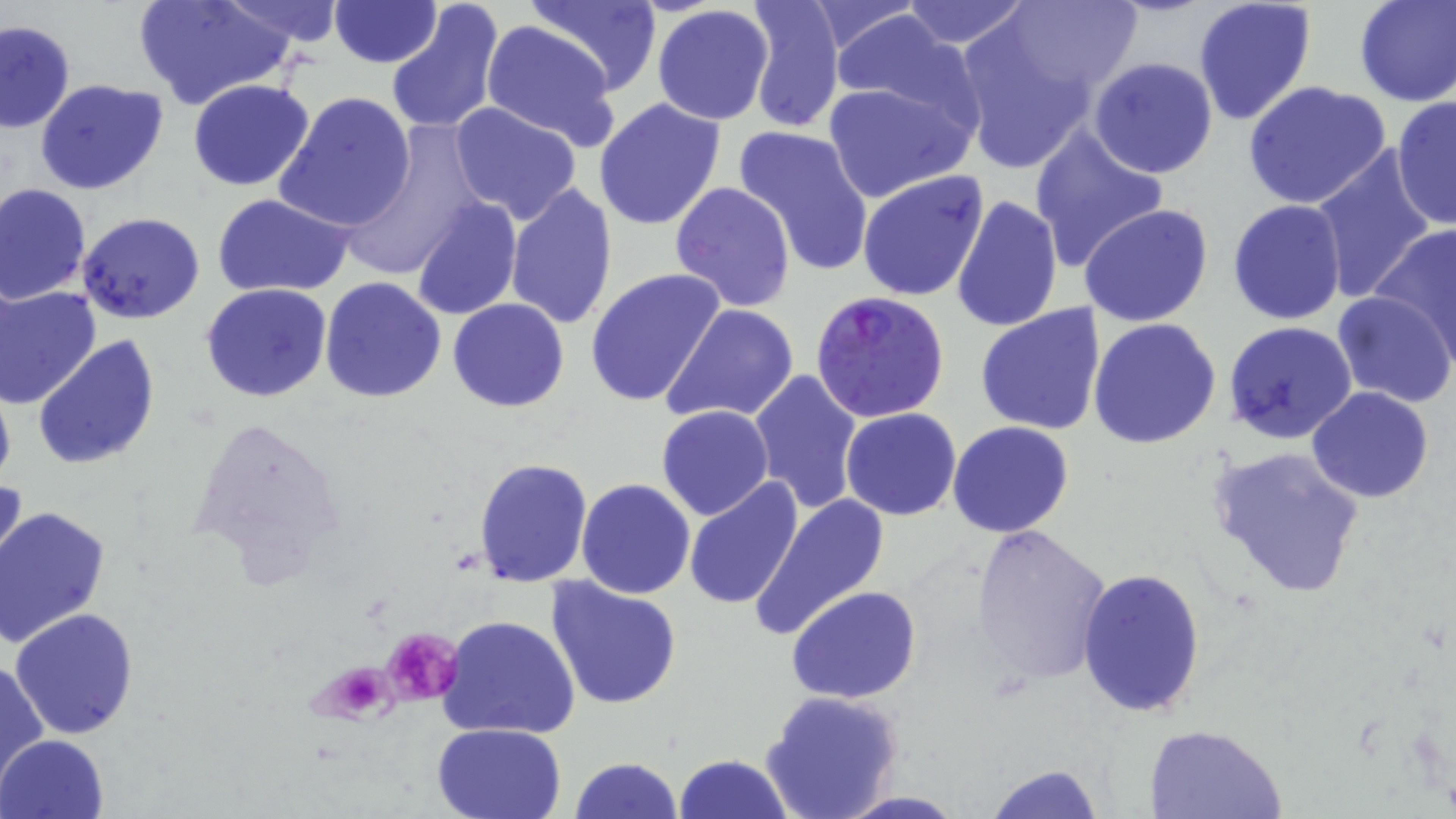

slide-level diagnosis = Plasmodium falciparum
stain = May-Grünwald-Giemsa
platelet locations = approximate bounding boxes as named x1/y1/x2/y2 corners in pixels: (x1=381, y1=625, x2=463, y2=707), (x1=315, y1=660, x2=397, y2=726)
modality = light microscopy
field of view = one of a larger specimen
image size = 1456×819 pixels
uninfected red blood cell locations = approximate bounding boxes as named x1/y1/x2/y2 corners in pixels: (x1=135, y1=0, x2=294, y2=112), (x1=221, y1=0, x2=345, y2=47), (x1=329, y1=0, x2=441, y2=68), (x1=385, y1=0, x2=507, y2=137), (x1=527, y1=0, x2=661, y2=94), (x1=744, y1=0, x2=844, y2=133), (x1=898, y1=0, x2=1034, y2=48), (x1=1193, y1=0, x2=1318, y2=126), (x1=1354, y1=0, x2=1455, y2=105), (x1=802, y1=1, x2=927, y2=58), (x1=988, y1=1, x2=1143, y2=99), (x1=651, y1=4, x2=775, y2=125), (x1=828, y1=8, x2=979, y2=127), (x1=479, y1=16, x2=620, y2=150), (x1=950, y1=16, x2=1103, y2=177), (x1=0, y1=18, x2=74, y2=134), (x1=1088, y1=57, x2=1218, y2=179), (x1=35, y1=79, x2=168, y2=197), (x1=187, y1=79, x2=316, y2=191), (x1=822, y1=80, x2=974, y2=201), (x1=1244, y1=82, x2=1393, y2=211), (x1=275, y1=90, x2=415, y2=232), (x1=1392, y1=94, x2=1455, y2=233), (x1=593, y1=97, x2=727, y2=232), (x1=447, y1=102, x2=584, y2=225), (x1=336, y1=121, x2=490, y2=284), (x1=730, y1=123, x2=876, y2=277), (x1=1027, y1=127, x2=1169, y2=270), (x1=1310, y1=147, x2=1440, y2=304), (x1=857, y1=170, x2=990, y2=302), (x1=0, y1=182, x2=91, y2=304), (x1=504, y1=182, x2=618, y2=330), (x1=669, y1=182, x2=797, y2=312), (x1=212, y1=193, x2=355, y2=296), (x1=952, y1=194, x2=1062, y2=335), (x1=411, y1=199, x2=523, y2=320), (x1=1226, y1=199, x2=1347, y2=324), (x1=1080, y1=203, x2=1212, y2=326), (x1=77, y1=213, x2=205, y2=324), (x1=1369, y1=222, x2=1456, y2=361), (x1=584, y1=269, x2=723, y2=409), (x1=319, y1=276, x2=448, y2=404), (x1=201, y1=283, x2=332, y2=403), (x1=0, y1=285, x2=101, y2=408), (x1=1333, y1=290, x2=1455, y2=408), (x1=447, y1=299, x2=570, y2=413), (x1=975, y1=303, x2=1108, y2=435), (x1=663, y1=304, x2=802, y2=425), (x1=1087, y1=318, x2=1221, y2=448), (x1=1224, y1=321, x2=1356, y2=445), (x1=33, y1=335, x2=161, y2=470), (x1=749, y1=369, x2=863, y2=513), (x1=0, y1=376, x2=15, y2=496), (x1=1307, y1=386, x2=1434, y2=503), (x1=656, y1=405, x2=775, y2=520), (x1=841, y1=407, x2=962, y2=521), (x1=186, y1=412, x2=348, y2=589), (x1=948, y1=421, x2=1073, y2=537), (x1=1206, y1=444, x2=1367, y2=599), (x1=473, y1=457, x2=594, y2=588), (x1=1, y1=475, x2=28, y2=591), (x1=682, y1=477, x2=803, y2=611), (x1=577, y1=478, x2=696, y2=599), (x1=749, y1=492, x2=890, y2=640), (x1=0, y1=505, x2=110, y2=649), (x1=970, y1=523, x2=1113, y2=687), (x1=1078, y1=565, x2=1206, y2=718), (x1=545, y1=578, x2=681, y2=709), (x1=787, y1=584, x2=922, y2=704), (x1=10, y1=608, x2=140, y2=740), (x1=436, y1=613, x2=582, y2=743), (x1=1, y1=660, x2=47, y2=784), (x1=759, y1=689, x2=904, y2=819), (x1=431, y1=721, x2=568, y2=818), (x1=1143, y1=723, x2=1285, y2=818), (x1=1, y1=733, x2=108, y2=818), (x1=673, y1=753, x2=795, y2=819), (x1=569, y1=757, x2=684, y2=819), (x1=981, y1=762, x2=1104, y2=819)
magnification = 1000x
Plasmodium falciparum-infected red blood cell locations = approximate bounding boxes as named x1/y1/x2/y2 corners in pixels: (x1=808, y1=291, x2=952, y2=426)
preparation = thin blood smear